Identify the parasite.
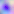
Toxoplasma gondii.

magnification: 400x
modality: photomicrograph